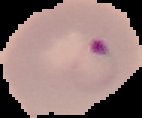 Malaria status: parasitized. Image is 142×118 pixels. Segmented cell region on a black background. From a thin blood film.